Assess this cell for malaria.
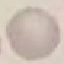

Uninfected.

Summary:
  - Preparation: thin blood film
  - Stain: Giemsa
  - Capture: smartphone through the microscope eyepiece
  - Image type: cell patch, automatically extracted from a larger field of view and resized to 64 × 64 pixels